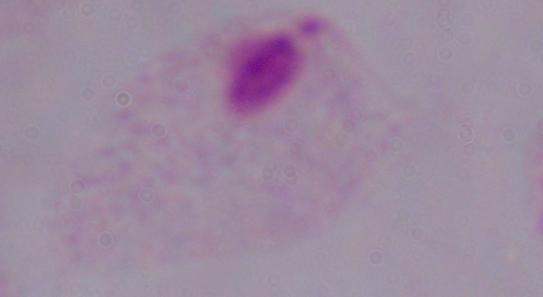 Photomicrograph. A trichomonad is shown. Captured at 1000x magnification.